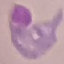
Malaria status: parasitized. Acquired by smartphone through the microscope eyepiece. Thin blood smear. Cell patch, automatically extracted from a larger field of view and resized to 64 × 64 pixels. Giemsa-stained preparation.